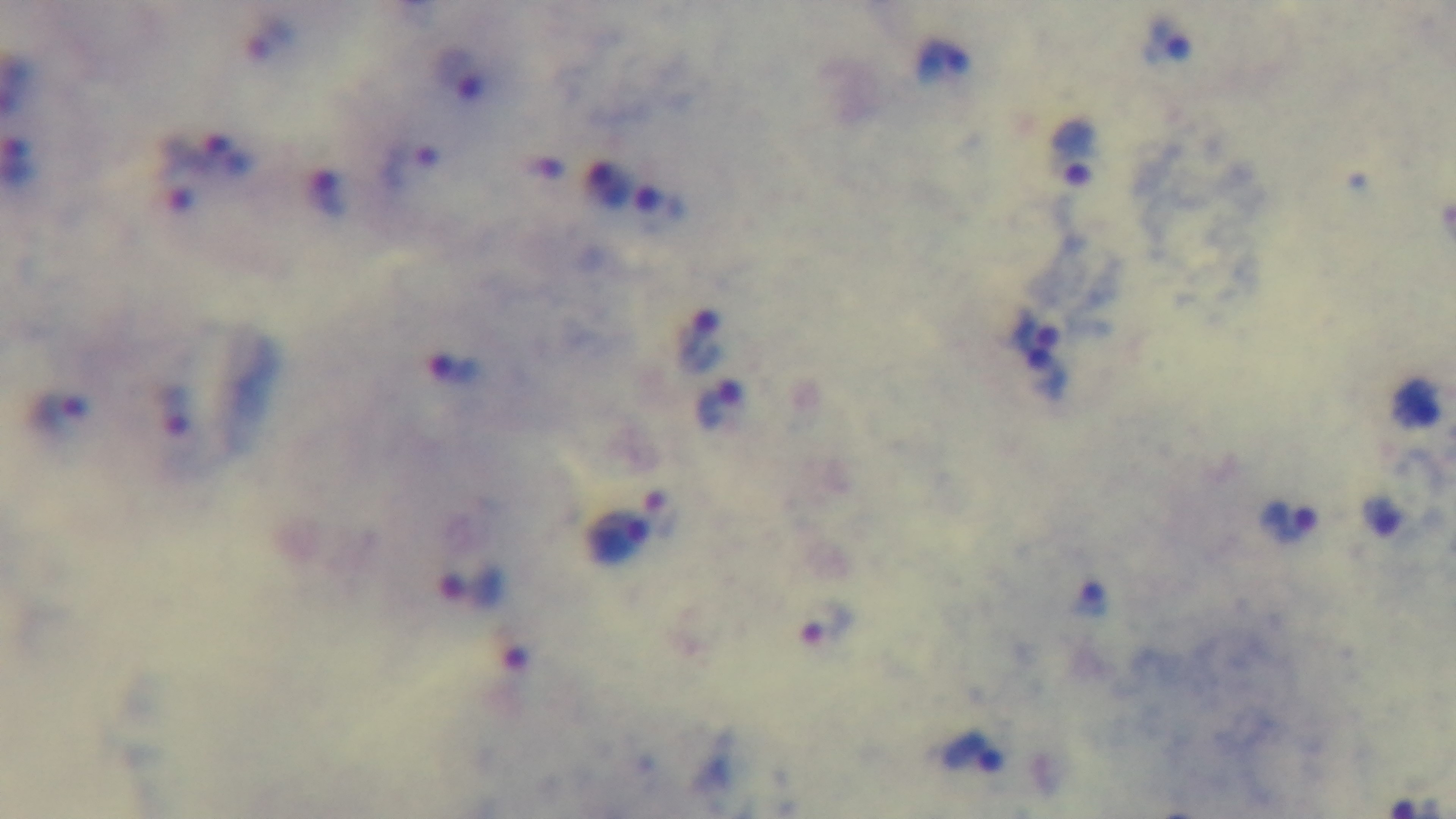

{
  "malaria_status": "infected",
  "modality": "light microscopy",
  "field_of_view": "one from the slide",
  "capture": "mounted 4K digital camera",
  "objective": "100x oil immersion",
  "stain": "Giemsa",
  "preparation": "thick smear"
}